Locate every leukocyte (white blood cell).
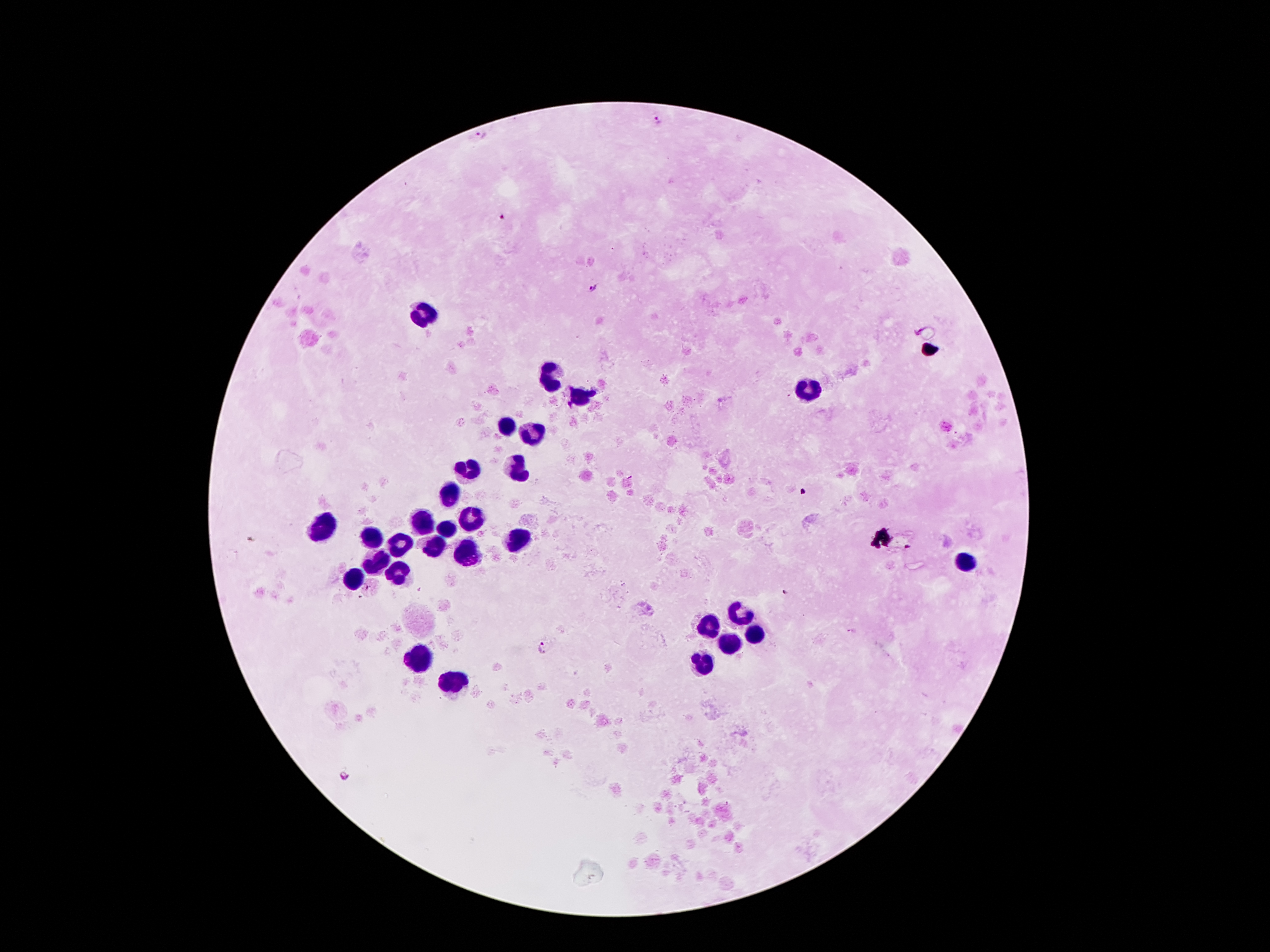

Approximate centers as (x, y) in pixels.
Leukocytes: (424, 313), (550, 376), (814, 386), (580, 395), (506, 421), (529, 432), (472, 467), (517, 467), (449, 496), (468, 516), (422, 523), (321, 530), (446, 530), (372, 540), (516, 540), (400, 542), (432, 547), (468, 552), (374, 559), (964, 563), (396, 571), (353, 582), (737, 611), (710, 624), (753, 633), (729, 641), (418, 657), (703, 664), (448, 683).

Summary:
  - Plasmodium parasite locations: (656, 120), (479, 134), (500, 218), (594, 288), (907, 548), (786, 594), (545, 648), (343, 777)
  - Image size: 1270×952 pixels
  - Field of view: single
  - Stain: Giemsa
  - Patient malaria status: positive for Plasmodium falciparum
  - Capture: smartphone through the microscope eyepiece
  - Preparation: thick blood smear
  - Magnification: 100x